Report the malaria status of this cell.
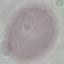
It is uninfected.

Photographed with a smartphone camera at the microscope eyepiece. Giemsa-stained preparation. Thin blood smear. Cell patch, automatically extracted from a larger field of view and resized to 64 × 64 pixels.